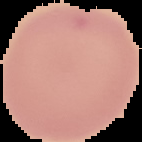

From a thin blood smear. Result: no Plasmodium parasites seen. Image is 142×142 pixels. The area outside the segmented cell region is set to black.